Describe the morphology of the erythrocytes.
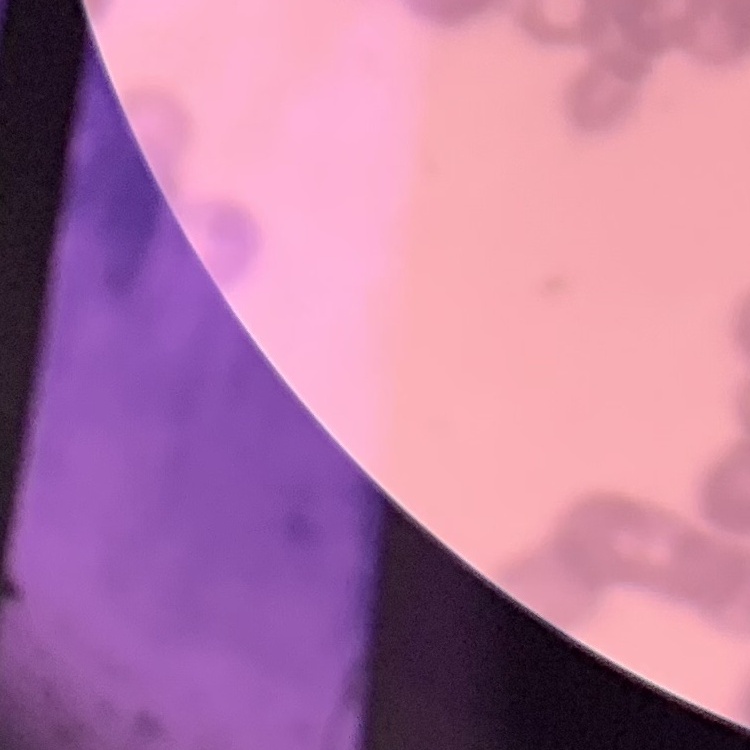
They show rouleaux formation.

Summary:
  - Stain: Field's or Giemsa
  - Image type: square crop of a larger photomicrograph
  - Preparation: thin blood film